Give the position of every Plasmodium parasite visible.
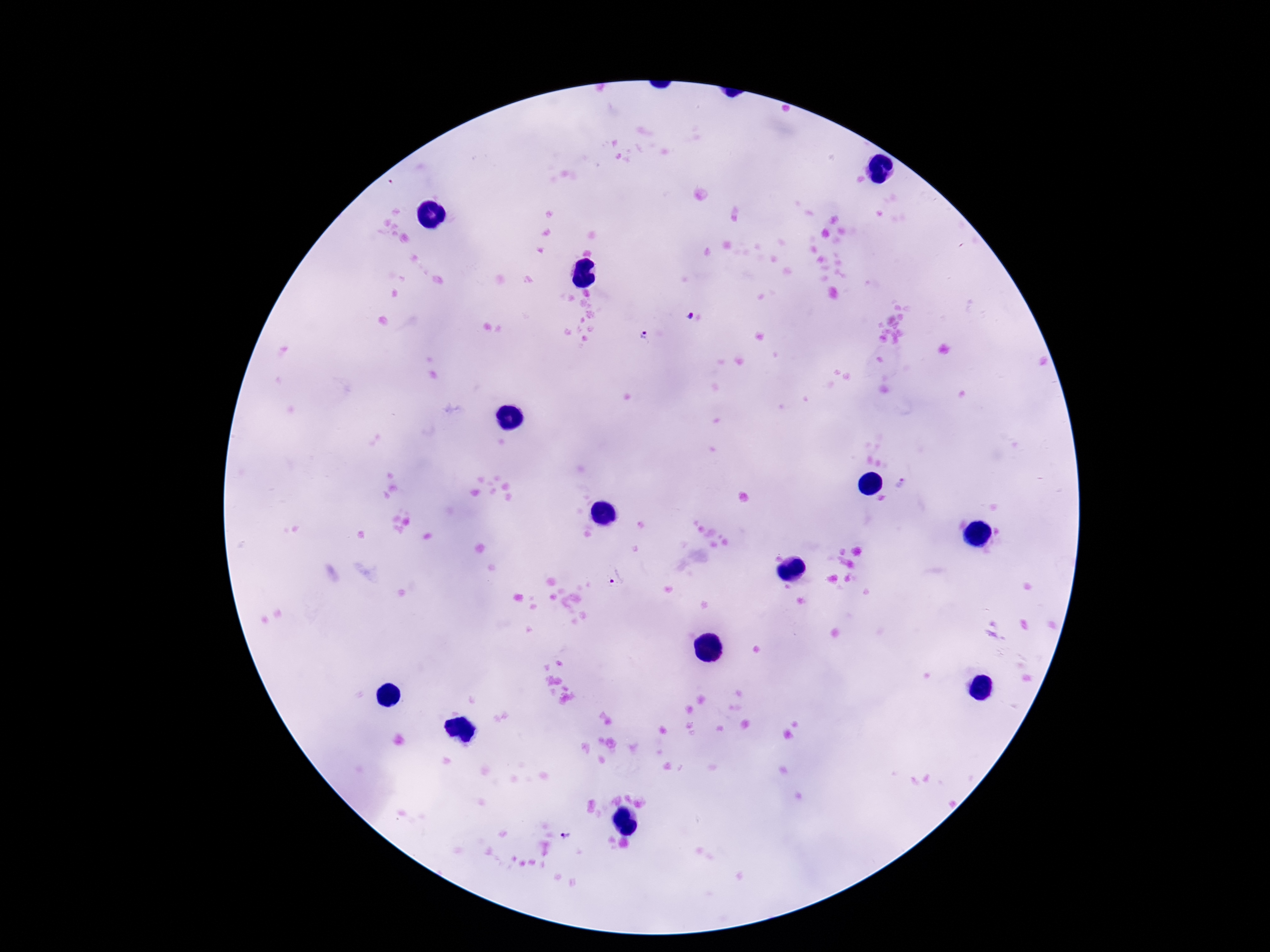
Approximate centers as {x, y} in pixels.
Plasmodium parasites: {688, 315}, {644, 335}, {901, 482}, {616, 578}, {568, 835}.

magnification: 100x
image_size: 1270×952 pixels
patient_malaria_status: infected
preparation: thick blood film
capture: smartphone camera through the microscope eyepiece
stain: Giemsa
field_of_view: single